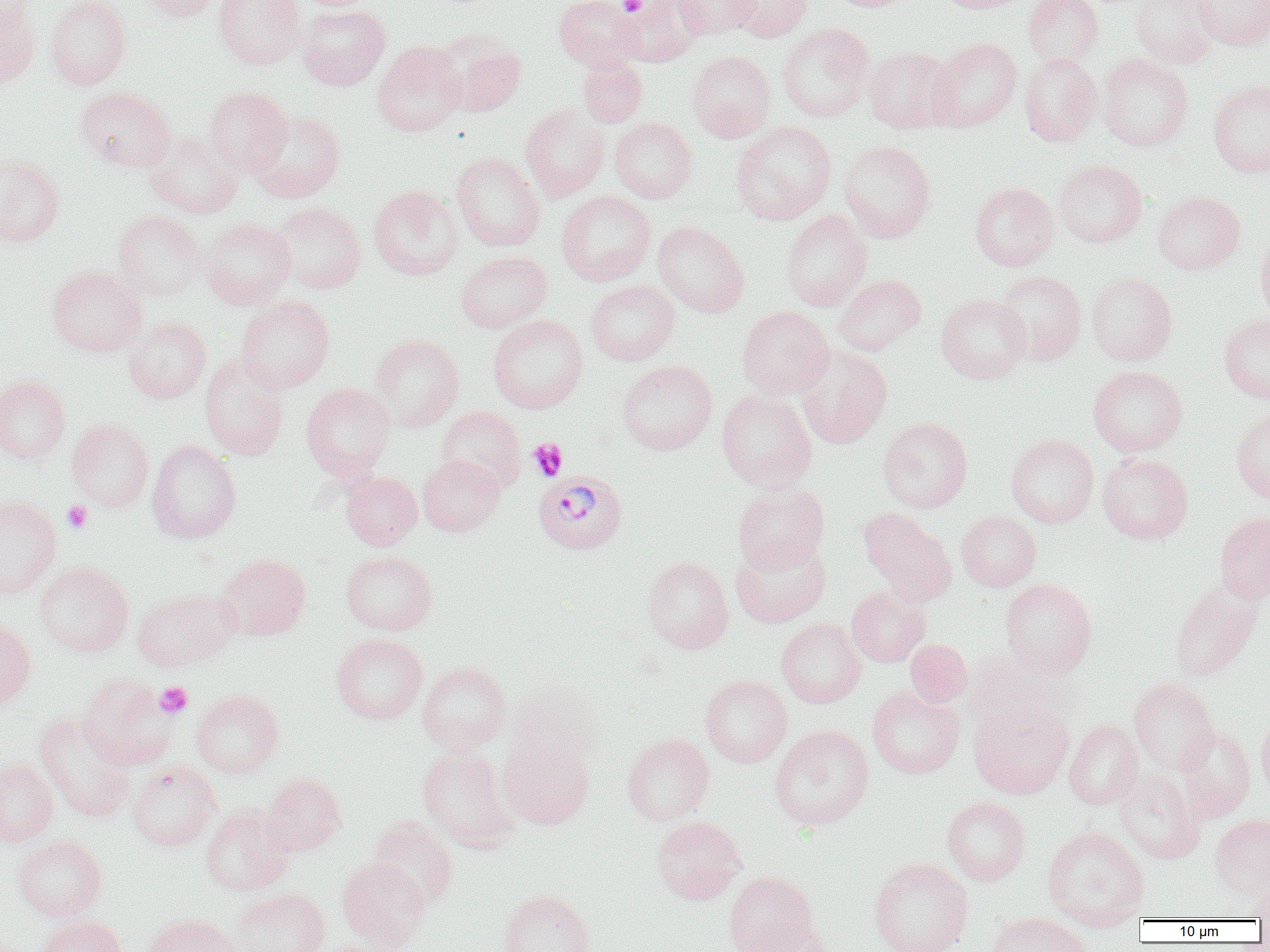
Summary:
  - Coordinate format: approximate bounding boxes as named x1/y1/x2/y2 corners in pixels
  - Uninfected red blood cell locations: (x1=134, y1=0, x2=222, y2=21), (x1=214, y1=0, x2=305, y2=69), (x1=554, y1=0, x2=644, y2=71), (x1=619, y1=0, x2=707, y2=66), (x1=673, y1=0, x2=759, y2=39), (x1=725, y1=0, x2=814, y2=42), (x1=824, y1=0, x2=921, y2=12), (x1=935, y1=0, x2=1034, y2=13), (x1=1023, y1=0, x2=1104, y2=68), (x1=1130, y1=0, x2=1220, y2=68), (x1=1189, y1=0, x2=1269, y2=50), (x1=0, y1=1, x2=41, y2=89), (x1=45, y1=1, x2=131, y2=90), (x1=298, y1=4, x2=391, y2=90), (x1=777, y1=23, x2=875, y2=122), (x1=436, y1=30, x2=527, y2=118), (x1=928, y1=37, x2=1022, y2=132), (x1=373, y1=41, x2=466, y2=136), (x1=864, y1=45, x2=957, y2=133), (x1=687, y1=50, x2=776, y2=142), (x1=1019, y1=52, x2=1102, y2=147), (x1=1098, y1=53, x2=1193, y2=151), (x1=578, y1=55, x2=647, y2=128), (x1=1208, y1=78, x2=1270, y2=178), (x1=75, y1=86, x2=175, y2=173), (x1=204, y1=86, x2=292, y2=175), (x1=520, y1=103, x2=610, y2=203), (x1=249, y1=111, x2=345, y2=202), (x1=609, y1=117, x2=696, y2=203), (x1=731, y1=121, x2=837, y2=225), (x1=144, y1=131, x2=243, y2=218), (x1=839, y1=140, x2=936, y2=243), (x1=452, y1=151, x2=546, y2=251), (x1=0, y1=154, x2=65, y2=247), (x1=1053, y1=159, x2=1147, y2=248), (x1=969, y1=182, x2=1058, y2=271), (x1=369, y1=185, x2=463, y2=280), (x1=1152, y1=190, x2=1246, y2=274), (x1=556, y1=191, x2=656, y2=286), (x1=270, y1=202, x2=366, y2=294), (x1=112, y1=209, x2=208, y2=300), (x1=782, y1=209, x2=872, y2=311), (x1=199, y1=217, x2=296, y2=309), (x1=652, y1=220, x2=749, y2=317), (x1=1255, y1=230, x2=1270, y2=327), (x1=456, y1=251, x2=552, y2=333), (x1=47, y1=266, x2=146, y2=357), (x1=993, y1=270, x2=1087, y2=365), (x1=1087, y1=271, x2=1177, y2=366), (x1=834, y1=274, x2=926, y2=356), (x1=585, y1=279, x2=680, y2=365), (x1=935, y1=294, x2=1030, y2=384), (x1=235, y1=295, x2=335, y2=394), (x1=737, y1=306, x2=834, y2=398), (x1=1219, y1=313, x2=1270, y2=405), (x1=487, y1=314, x2=587, y2=414), (x1=123, y1=316, x2=211, y2=404), (x1=369, y1=333, x2=464, y2=431), (x1=795, y1=345, x2=892, y2=449), (x1=199, y1=353, x2=289, y2=461), (x1=616, y1=360, x2=717, y2=455), (x1=1088, y1=365, x2=1188, y2=456), (x1=0, y1=375, x2=71, y2=464), (x1=301, y1=383, x2=395, y2=480), (x1=717, y1=388, x2=817, y2=491), (x1=436, y1=406, x2=526, y2=494), (x1=1231, y1=406, x2=1270, y2=504), (x1=878, y1=417, x2=973, y2=513), (x1=67, y1=418, x2=154, y2=511), (x1=1005, y1=433, x2=1098, y2=528), (x1=147, y1=440, x2=242, y2=543), (x1=1006, y1=443, x2=1193, y2=534), (x1=1098, y1=453, x2=1193, y2=545), (x1=418, y1=455, x2=504, y2=536), (x1=340, y1=470, x2=422, y2=549), (x1=732, y1=482, x2=829, y2=572), (x1=0, y1=495, x2=61, y2=597), (x1=859, y1=509, x2=956, y2=606), (x1=956, y1=510, x2=1041, y2=591), (x1=1214, y1=512, x2=1270, y2=604), (x1=731, y1=537, x2=831, y2=628), (x1=341, y1=551, x2=438, y2=636), (x1=215, y1=553, x2=311, y2=641), (x1=642, y1=556, x2=734, y2=653), (x1=34, y1=561, x2=134, y2=657), (x1=999, y1=578, x2=1097, y2=678), (x1=1168, y1=581, x2=1263, y2=682), (x1=846, y1=586, x2=930, y2=667), (x1=133, y1=588, x2=238, y2=671), (x1=0, y1=617, x2=36, y2=710), (x1=776, y1=618, x2=866, y2=707), (x1=331, y1=633, x2=428, y2=724), (x1=905, y1=639, x2=972, y2=707), (x1=965, y1=647, x2=1076, y2=735), (x1=417, y1=661, x2=511, y2=754), (x1=78, y1=674, x2=176, y2=769), (x1=700, y1=675, x2=792, y2=768), (x1=1128, y1=677, x2=1219, y2=774), (x1=507, y1=683, x2=602, y2=772), (x1=866, y1=686, x2=964, y2=779), (x1=191, y1=689, x2=283, y2=778), (x1=968, y1=700, x2=1073, y2=799), (x1=34, y1=712, x2=136, y2=822), (x1=1256, y1=712, x2=1270, y2=800), (x1=1064, y1=719, x2=1144, y2=810), (x1=769, y1=725, x2=874, y2=830), (x1=1174, y1=726, x2=1256, y2=822), (x1=621, y1=732, x2=715, y2=825), (x1=497, y1=738, x2=594, y2=829), (x1=417, y1=746, x2=518, y2=851), (x1=0, y1=758, x2=58, y2=846), (x1=126, y1=761, x2=220, y2=851), (x1=1113, y1=770, x2=1204, y2=864), (x1=262, y1=773, x2=347, y2=856), (x1=941, y1=796, x2=1031, y2=886), (x1=200, y1=805, x2=293, y2=896), (x1=1209, y1=813, x2=1270, y2=898), (x1=368, y1=815, x2=458, y2=909), (x1=651, y1=816, x2=747, y2=904), (x1=1042, y1=826, x2=1149, y2=930), (x1=12, y1=834, x2=108, y2=920), (x1=337, y1=857, x2=430, y2=950), (x1=868, y1=857, x2=974, y2=952), (x1=724, y1=871, x2=818, y2=951), (x1=1248, y1=881, x2=1270, y2=922), (x1=230, y1=887, x2=330, y2=952), (x1=497, y1=889, x2=595, y2=952), (x1=986, y1=911, x2=1092, y2=952), (x1=143, y1=913, x2=241, y2=952), (x1=39, y1=914, x2=128, y2=952), (x1=740, y1=921, x2=835, y2=952)
  - Platelet locations: (x1=619, y1=0, x2=646, y2=16), (x1=528, y1=438, x2=568, y2=481), (x1=62, y1=500, x2=93, y2=534), (x1=155, y1=682, x2=193, y2=719)
  - Plasmodium vivax-infected red blood cell locations: (x1=533, y1=470, x2=627, y2=555)
  - Slide-level diagnosis: Plasmodium vivax
  - Field of view: single
  - Modality: light microscopy
  - Magnification: 1000x
  - Preparation: thin blood smear
  - Image size: 1270×952 pixels